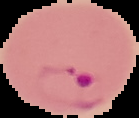

Summary:
  - Preparation: thin blood film
  - Image type: segmented cell region with the area outside set to black
  - Image size: 139×118 pixels
  - Malaria status: parasitized